Identify the cell.
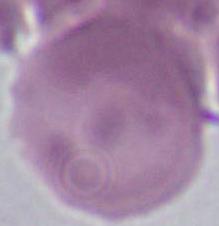

An erythrocyte.

modality = micrograph
magnification = 1000x